State which parasite is depicted.
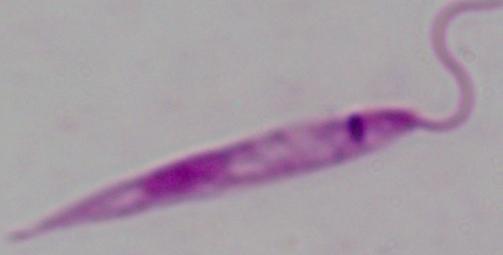
Leishmania.

Summary:
  - Magnification: 1000x
  - Modality: micrograph